Assess this cell for malaria.
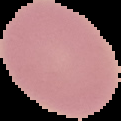
It is uninfected.

From a thin blood smear. Image is 121×121 pixels. The area outside the segmented cell region is set to black.